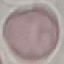
result: no malaria parasites seen
capture: smartphone camera at the microscope eyepiece
preparation: thin smear
stain: Giemsa
image_type: automatically extracted cell patch, resized to 64 × 64 pixels